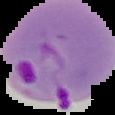

Summary:
  - Image type: segmented cell region on a black background
  - Image size: 115×115 pixels
  - Preparation: thin blood film
  - Result: malaria parasites identified